Name the blood parasite species.
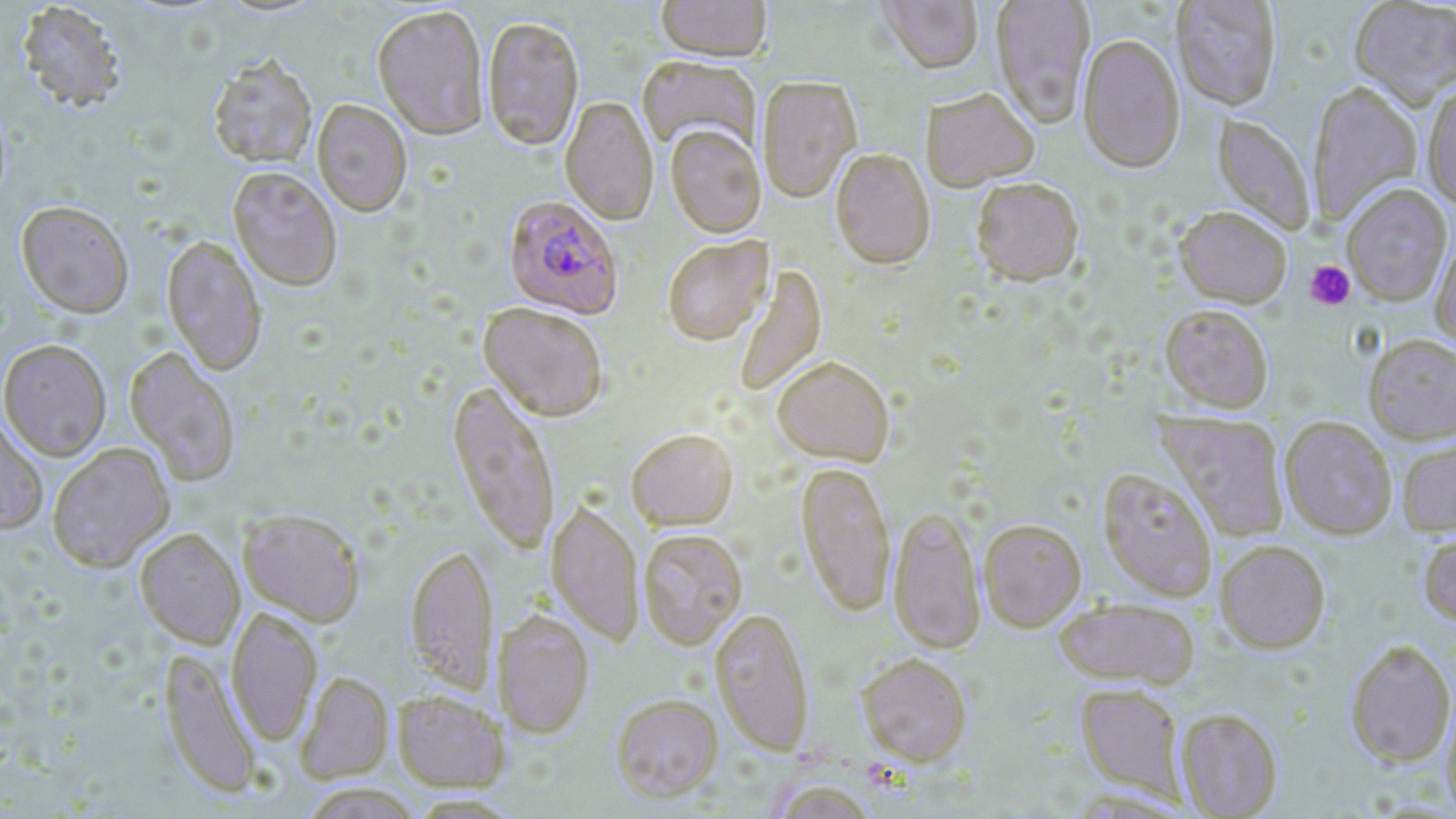
Plasmodium falciparum.

Approximate bounding boxes as (x1, y1, x2, y2) in pixels. Plasmodium falciparum-infected red blood cell locations: (502, 198, 623, 321). Uninfected red blood cell locations: (215, 0, 328, 19), (656, 0, 772, 65), (875, 0, 983, 77), (991, 0, 1095, 130), (1172, 0, 1282, 113), (1348, 0, 1456, 112), (15, 2, 127, 113), (372, 8, 489, 144), (482, 19, 584, 154), (1078, 36, 1186, 176), (637, 57, 760, 155), (207, 60, 317, 172), (757, 78, 862, 205), (1308, 83, 1423, 226), (1423, 86, 1456, 212), (921, 90, 1040, 194), (560, 98, 658, 227), (312, 100, 412, 219), (1212, 115, 1315, 236), (665, 127, 766, 241), (830, 151, 935, 272), (227, 168, 342, 293), (972, 181, 1084, 289), (1342, 186, 1452, 306), (16, 204, 134, 321), (1174, 208, 1291, 309), (161, 236, 266, 377), (1431, 236, 1456, 356), (663, 238, 774, 348), (733, 264, 827, 397), (478, 305, 607, 423), (1160, 306, 1273, 415), (1363, 335, 1456, 446), (0, 340, 111, 462), (124, 347, 240, 487), (772, 359, 894, 469), (445, 382, 560, 556), (1158, 412, 1289, 542), (0, 413, 49, 536), (1280, 417, 1397, 541), (626, 432, 738, 533), (1397, 437, 1456, 537), (48, 443, 175, 573), (795, 464, 895, 618), (1098, 470, 1217, 603), (546, 502, 644, 648), (889, 509, 985, 656), (237, 510, 366, 629), (979, 520, 1087, 633), (135, 529, 245, 650), (1419, 529, 1456, 629), (638, 531, 748, 651), (1215, 541, 1330, 654), (405, 548, 499, 698), (1054, 599, 1200, 690), (226, 608, 322, 747), (709, 609, 814, 757), (493, 612, 594, 739), (1345, 641, 1456, 768), (158, 647, 262, 800), (856, 654, 973, 768), (295, 672, 394, 784), (1075, 684, 1187, 801), (393, 691, 509, 792), (611, 695, 723, 804), (1442, 697, 1456, 819), (1175, 707, 1283, 818), (768, 780, 878, 819), (298, 783, 424, 819). Platelet locations: (1305, 260, 1355, 310). Captured at 1000x magnification. Single field of view. Light microscopy. Image is 1456×819 pixels. May-Grünwald-Giemsa-stained preparation. Thin blood film.